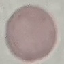
malaria status = uninfected
stain = Giemsa
image type = cell patch, automatically extracted from a larger field of view and resized to 64 × 64 pixels
preparation = thin smear
capture = smartphone camera at the microscope eyepiece